Report the malaria status of this cell.
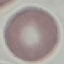

Uninfected.

capture = smartphone through the microscope eyepiece
preparation = thin blood film
stain = Giemsa
image type = cell patch, automatically extracted from a larger field of view and resized to 64 × 64 pixels